Outline each blood parasite and name the species.
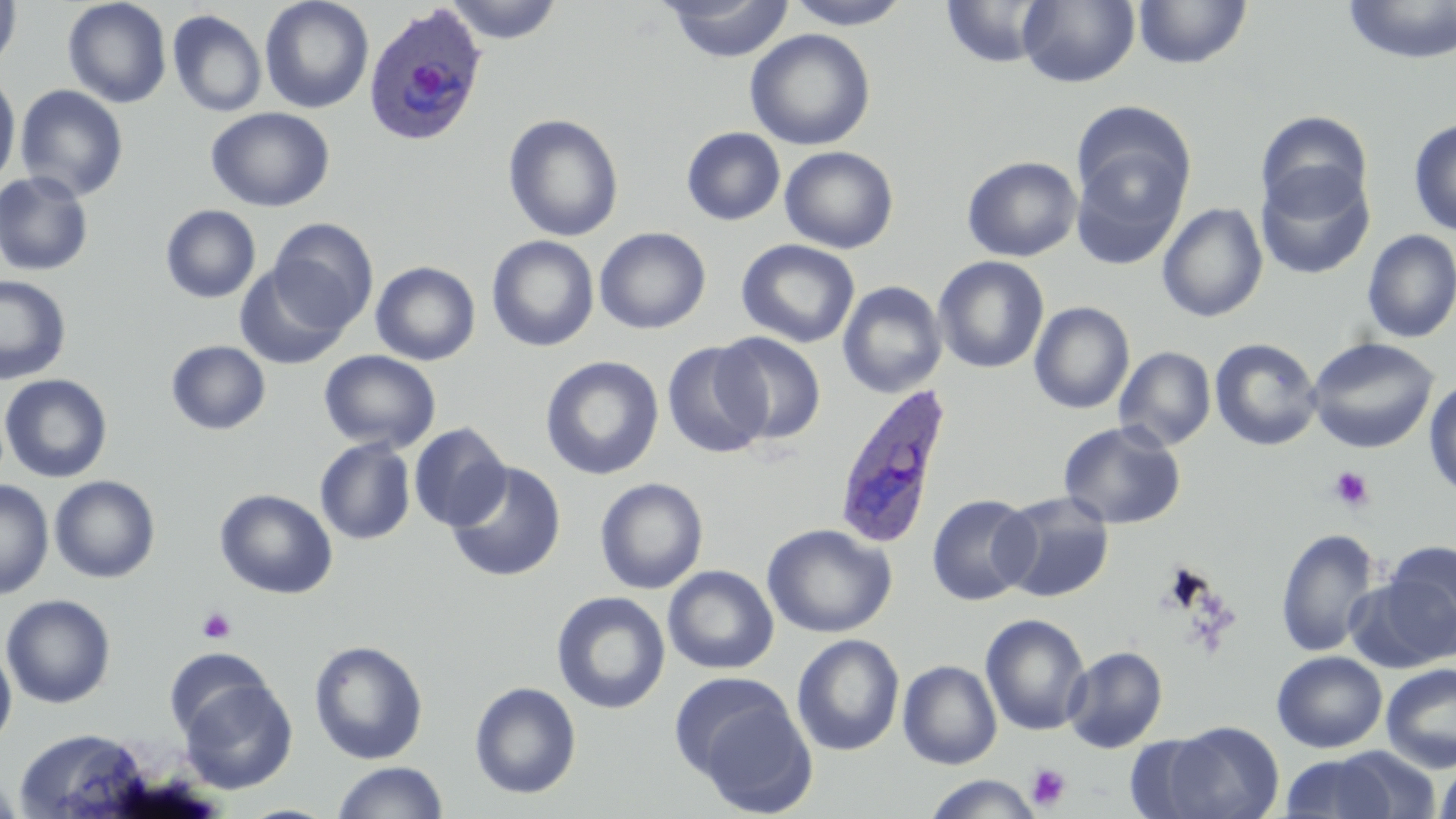
Approximate bounding boxes as (x1, y1, x2, y2) in pixels.
Plasmodium ovale-infected red blood cells: (363, 3, 490, 148), (830, 382, 954, 551).
No Plasmodium falciparum, Plasmodium malariae, Plasmodium vivax, Babesia divergens, or Trypanosoma brucei observed.

Platelet locations: (1328, 467, 1374, 513), (196, 607, 236, 643), (1025, 763, 1071, 810). Uninfected red blood cell locations: (0, 0, 22, 74), (62, 0, 172, 108), (259, 0, 374, 114), (444, 0, 564, 45), (786, 0, 910, 29), (1341, 0, 1456, 65), (660, 1, 795, 63), (941, 1, 1054, 68), (1018, 1, 1140, 88), (1132, 1, 1253, 70), (167, 9, 267, 117), (744, 29, 876, 151), (0, 71, 21, 189), (14, 85, 129, 202), (206, 107, 335, 213), (1070, 111, 1194, 262), (1255, 111, 1374, 219), (503, 114, 623, 242), (1408, 118, 1456, 236), (682, 126, 786, 226), (779, 145, 899, 254), (962, 155, 1082, 262), (1256, 164, 1375, 281), (0, 171, 94, 276), (1157, 203, 1268, 322), (160, 204, 260, 304), (268, 218, 378, 332), (594, 227, 711, 334), (1360, 229, 1456, 344), (486, 235, 599, 352), (736, 238, 860, 348), (933, 256, 1049, 374), (370, 261, 481, 365), (235, 264, 351, 370), (0, 274, 71, 385), (837, 281, 947, 399), (1029, 301, 1134, 414), (713, 332, 826, 445), (1209, 337, 1323, 451), (1306, 337, 1439, 454), (166, 341, 271, 435), (661, 341, 772, 459), (1114, 346, 1216, 451), (319, 350, 440, 453), (540, 355, 664, 480), (0, 373, 112, 483), (1424, 378, 1456, 499), (1058, 420, 1186, 530), (409, 422, 511, 531), (315, 438, 416, 545), (446, 461, 566, 582), (49, 475, 160, 583), (594, 477, 708, 594), (0, 480, 54, 599), (215, 489, 338, 599), (996, 492, 1116, 603), (926, 493, 1039, 606), (762, 523, 897, 639), (1276, 528, 1380, 657), (1375, 540, 1456, 663), (663, 565, 779, 675), (551, 591, 671, 714), (1, 594, 117, 709), (980, 613, 1091, 736), (791, 633, 905, 756), (0, 640, 17, 751), (309, 640, 429, 765), (1062, 645, 1168, 753), (162, 648, 275, 742), (1272, 651, 1387, 752), (897, 660, 1002, 770), (1381, 662, 1456, 773), (176, 676, 297, 795), (677, 679, 816, 814), (469, 681, 582, 799), (1160, 721, 1284, 818), (14, 727, 151, 818), (1326, 746, 1443, 818), (1279, 752, 1405, 819), (1435, 760, 1456, 819), (331, 761, 449, 819), (0, 771, 22, 819), (922, 775, 1044, 818). Slide-level diagnosis: Plasmodium ovale. Image is 1456×819 pixels. Optical microscopy. 1000x magnification. Thin blood smear. Single field of view. May-Grünwald-Giemsa-stained preparation.